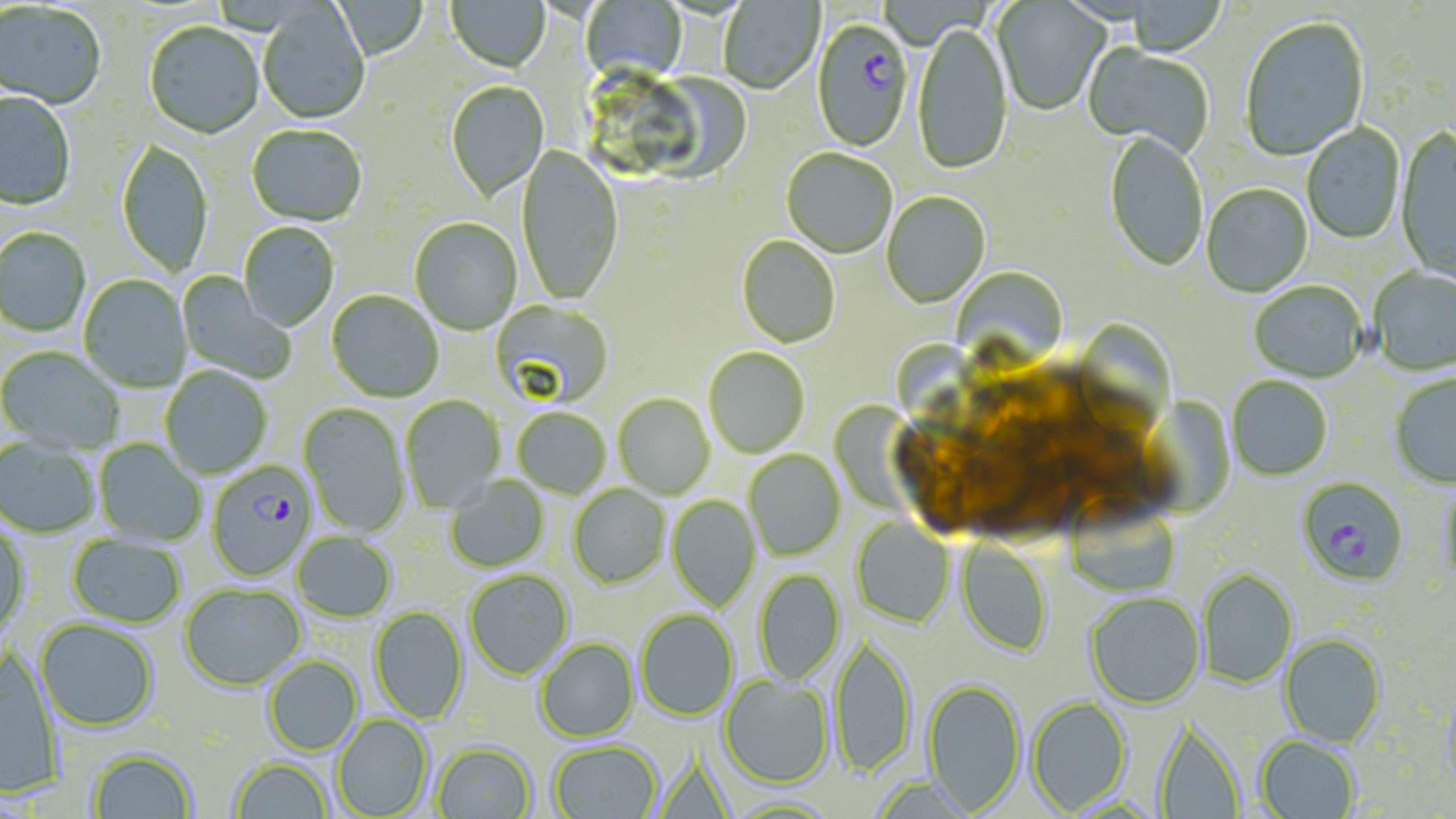 Approximate bounding boxes as named x1/y1/x2/y2 corners in pixels. Uninfected red blood cell locations: (x1=446, y1=0, x2=550, y2=74), (x1=581, y1=0, x2=688, y2=87), (x1=719, y1=0, x2=825, y2=96), (x1=331, y1=1, x2=429, y2=62), (x1=992, y1=1, x2=1111, y2=117), (x1=1126, y1=1, x2=1226, y2=58), (x1=0, y1=3, x2=106, y2=111), (x1=257, y1=4, x2=370, y2=126), (x1=1240, y1=18, x2=1370, y2=162), (x1=145, y1=23, x2=265, y2=140), (x1=913, y1=25, x2=1013, y2=178), (x1=1082, y1=45, x2=1214, y2=158), (x1=446, y1=82, x2=549, y2=203), (x1=0, y1=93, x2=76, y2=211), (x1=1301, y1=123, x2=1405, y2=246), (x1=246, y1=126, x2=367, y2=227), (x1=1395, y1=129, x2=1456, y2=284), (x1=1104, y1=133, x2=1208, y2=274), (x1=116, y1=140, x2=213, y2=280), (x1=516, y1=146, x2=624, y2=307), (x1=781, y1=149, x2=897, y2=259), (x1=1201, y1=185, x2=1313, y2=298), (x1=882, y1=192, x2=991, y2=309), (x1=409, y1=218, x2=522, y2=336), (x1=239, y1=224, x2=339, y2=332), (x1=0, y1=229, x2=92, y2=337), (x1=736, y1=236, x2=840, y2=349), (x1=951, y1=267, x2=1068, y2=371), (x1=1369, y1=268, x2=1456, y2=377), (x1=176, y1=271, x2=296, y2=384), (x1=79, y1=275, x2=191, y2=393), (x1=1249, y1=283, x2=1367, y2=384), (x1=326, y1=291, x2=444, y2=403), (x1=489, y1=300, x2=614, y2=411), (x1=1071, y1=320, x2=1176, y2=435), (x1=894, y1=344, x2=1003, y2=451), (x1=0, y1=347, x2=125, y2=454), (x1=703, y1=348, x2=810, y2=459), (x1=160, y1=367, x2=272, y2=479), (x1=1389, y1=374, x2=1456, y2=489), (x1=1227, y1=377, x2=1333, y2=481), (x1=1136, y1=389, x2=1232, y2=511), (x1=613, y1=393, x2=715, y2=500), (x1=400, y1=395, x2=505, y2=512), (x1=298, y1=402, x2=410, y2=537), (x1=835, y1=403, x2=942, y2=509), (x1=512, y1=408, x2=611, y2=499), (x1=0, y1=438, x2=100, y2=539), (x1=94, y1=439, x2=206, y2=547), (x1=744, y1=450, x2=845, y2=561), (x1=445, y1=476, x2=550, y2=572), (x1=1439, y1=481, x2=1456, y2=591), (x1=568, y1=485, x2=670, y2=589), (x1=666, y1=495, x2=761, y2=610), (x1=1067, y1=499, x2=1181, y2=598), (x1=851, y1=516, x2=955, y2=628), (x1=0, y1=522, x2=31, y2=636), (x1=292, y1=532, x2=397, y2=624), (x1=67, y1=534, x2=186, y2=628), (x1=956, y1=540, x2=1052, y2=657), (x1=753, y1=568, x2=845, y2=685), (x1=1196, y1=568, x2=1299, y2=689), (x1=464, y1=570, x2=574, y2=680), (x1=179, y1=584, x2=306, y2=692), (x1=1085, y1=593, x2=1205, y2=709), (x1=369, y1=606, x2=469, y2=724), (x1=635, y1=609, x2=738, y2=721), (x1=35, y1=620, x2=159, y2=733), (x1=1279, y1=633, x2=1387, y2=747), (x1=831, y1=635, x2=917, y2=779), (x1=534, y1=638, x2=639, y2=742), (x1=0, y1=649, x2=64, y2=798), (x1=263, y1=656, x2=364, y2=757), (x1=719, y1=675, x2=834, y2=788), (x1=921, y1=678, x2=1026, y2=813), (x1=1439, y1=686, x2=1456, y2=796), (x1=1026, y1=697, x2=1133, y2=815), (x1=332, y1=714, x2=434, y2=819), (x1=1152, y1=719, x2=1246, y2=818), (x1=1255, y1=735, x2=1359, y2=819), (x1=549, y1=741, x2=662, y2=819), (x1=431, y1=742, x2=537, y2=819), (x1=86, y1=747, x2=198, y2=818), (x1=230, y1=758, x2=333, y2=819). Plasmodium falciparum-infected red blood cell locations: (x1=811, y1=21, x2=914, y2=155), (x1=206, y1=462, x2=317, y2=582), (x1=1296, y1=477, x2=1409, y2=588). Slide-level diagnosis: Plasmodium falciparum. Single field of view. Image is 1456×819 pixels. Light microscopy. Captured at 1000x magnification. Thin blood smear. May-Grünwald-Giemsa-stained preparation.